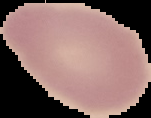
image type = cell region segmented out of the field of view; surrounding area masked to black
preparation = thin blood film
image size = 151×118 pixels
malaria status = uninfected